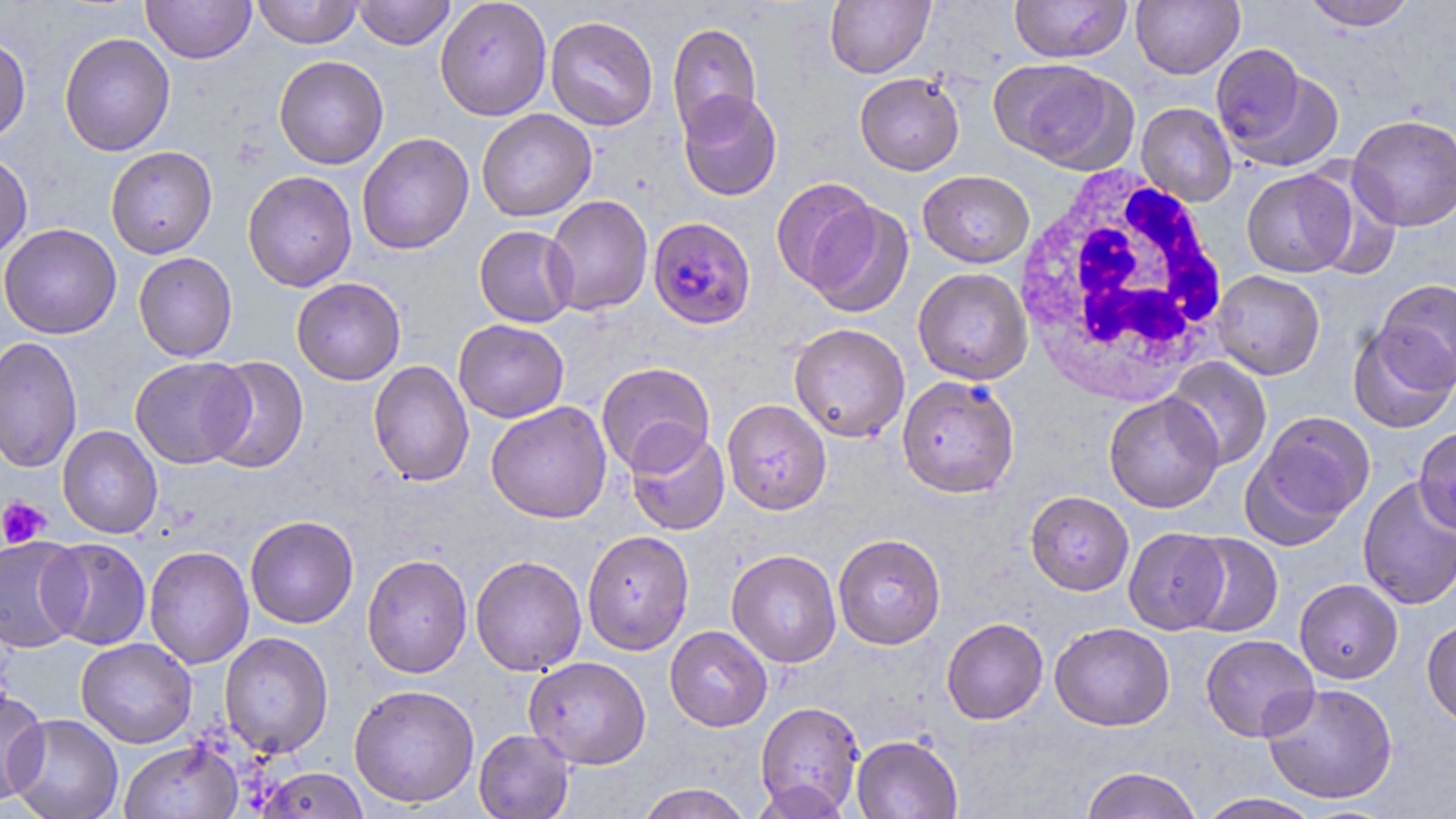
Summary:
  - Coordinate format: approximate bounding boxes as named x1/y1/x2/y2 corners in pixels
  - White blood cell locations: (x1=1012, y1=163, x2=1234, y2=403)
  - Uninfected red blood cell locations: (x1=141, y1=0, x2=256, y2=64), (x1=252, y1=0, x2=362, y2=48), (x1=353, y1=0, x2=455, y2=50), (x1=435, y1=0, x2=552, y2=121), (x1=824, y1=0, x2=935, y2=78), (x1=1009, y1=0, x2=1131, y2=63), (x1=1131, y1=0, x2=1245, y2=79), (x1=1301, y1=0, x2=1418, y2=31), (x1=545, y1=15, x2=659, y2=131), (x1=667, y1=22, x2=762, y2=137), (x1=59, y1=32, x2=176, y2=156), (x1=0, y1=34, x2=31, y2=144), (x1=274, y1=55, x2=389, y2=169), (x1=995, y1=59, x2=1135, y2=173), (x1=1219, y1=60, x2=1345, y2=173), (x1=854, y1=72, x2=964, y2=175), (x1=677, y1=89, x2=783, y2=201), (x1=1137, y1=102, x2=1237, y2=206), (x1=476, y1=109, x2=597, y2=222), (x1=1348, y1=114, x2=1456, y2=231), (x1=356, y1=133, x2=474, y2=255), (x1=105, y1=146, x2=217, y2=259), (x1=0, y1=153, x2=33, y2=262), (x1=1242, y1=169, x2=1356, y2=277), (x1=242, y1=170, x2=357, y2=293), (x1=918, y1=170, x2=1034, y2=268), (x1=769, y1=176, x2=881, y2=293), (x1=543, y1=195, x2=653, y2=316), (x1=804, y1=200, x2=914, y2=319), (x1=0, y1=223, x2=121, y2=340), (x1=474, y1=225, x2=578, y2=328), (x1=133, y1=252, x2=238, y2=362), (x1=913, y1=267, x2=1033, y2=386), (x1=1212, y1=270, x2=1325, y2=380), (x1=291, y1=277, x2=406, y2=385), (x1=1374, y1=278, x2=1456, y2=388), (x1=453, y1=319, x2=570, y2=423), (x1=788, y1=323, x2=910, y2=443), (x1=1348, y1=324, x2=1455, y2=433), (x1=0, y1=337, x2=83, y2=474), (x1=130, y1=356, x2=253, y2=469), (x1=201, y1=356, x2=310, y2=474), (x1=1165, y1=357, x2=1272, y2=471), (x1=368, y1=360, x2=475, y2=487), (x1=596, y1=362, x2=716, y2=475), (x1=897, y1=375, x2=1020, y2=498), (x1=1103, y1=392, x2=1223, y2=513), (x1=722, y1=399, x2=832, y2=515), (x1=486, y1=402, x2=612, y2=524), (x1=1247, y1=410, x2=1376, y2=539), (x1=57, y1=425, x2=163, y2=538), (x1=1413, y1=426, x2=1456, y2=533), (x1=625, y1=427, x2=730, y2=536), (x1=1357, y1=475, x2=1456, y2=610), (x1=1025, y1=490, x2=1134, y2=595), (x1=245, y1=515, x2=360, y2=629), (x1=1123, y1=527, x2=1229, y2=635), (x1=582, y1=530, x2=694, y2=655), (x1=833, y1=533, x2=946, y2=650), (x1=1181, y1=533, x2=1283, y2=637), (x1=0, y1=536, x2=86, y2=654), (x1=40, y1=538, x2=152, y2=650), (x1=144, y1=546, x2=254, y2=669), (x1=726, y1=550, x2=842, y2=668), (x1=361, y1=554, x2=472, y2=679), (x1=470, y1=555, x2=587, y2=676), (x1=1294, y1=579, x2=1403, y2=684), (x1=941, y1=618, x2=1049, y2=725), (x1=1422, y1=618, x2=1456, y2=728), (x1=1050, y1=622, x2=1175, y2=731), (x1=665, y1=626, x2=772, y2=731), (x1=219, y1=632, x2=334, y2=758), (x1=1200, y1=634, x2=1320, y2=742), (x1=76, y1=637, x2=197, y2=748), (x1=524, y1=656, x2=651, y2=769), (x1=1261, y1=681, x2=1398, y2=805), (x1=349, y1=684, x2=480, y2=809), (x1=0, y1=686, x2=48, y2=807), (x1=755, y1=701, x2=865, y2=816), (x1=6, y1=713, x2=123, y2=819), (x1=474, y1=729, x2=574, y2=819), (x1=851, y1=734, x2=962, y2=819), (x1=119, y1=740, x2=243, y2=819), (x1=1080, y1=766, x2=1203, y2=819), (x1=256, y1=767, x2=370, y2=819), (x1=749, y1=779, x2=852, y2=819), (x1=635, y1=783, x2=753, y2=819), (x1=1195, y1=793, x2=1323, y2=819)
  - Plasmodium falciparum-infected red blood cell locations: (x1=648, y1=216, x2=756, y2=330)
  - Platelet locations: (x1=0, y1=496, x2=51, y2=548)
  - Slide-level diagnosis: Plasmodium falciparum
  - Image size: 1456×819 pixels
  - Field of view: one of a larger specimen
  - Stain: May-Grünwald-Giemsa
  - Modality: light microscopy
  - Magnification: 1000x
  - Preparation: thin blood film